Mark where platelets are.
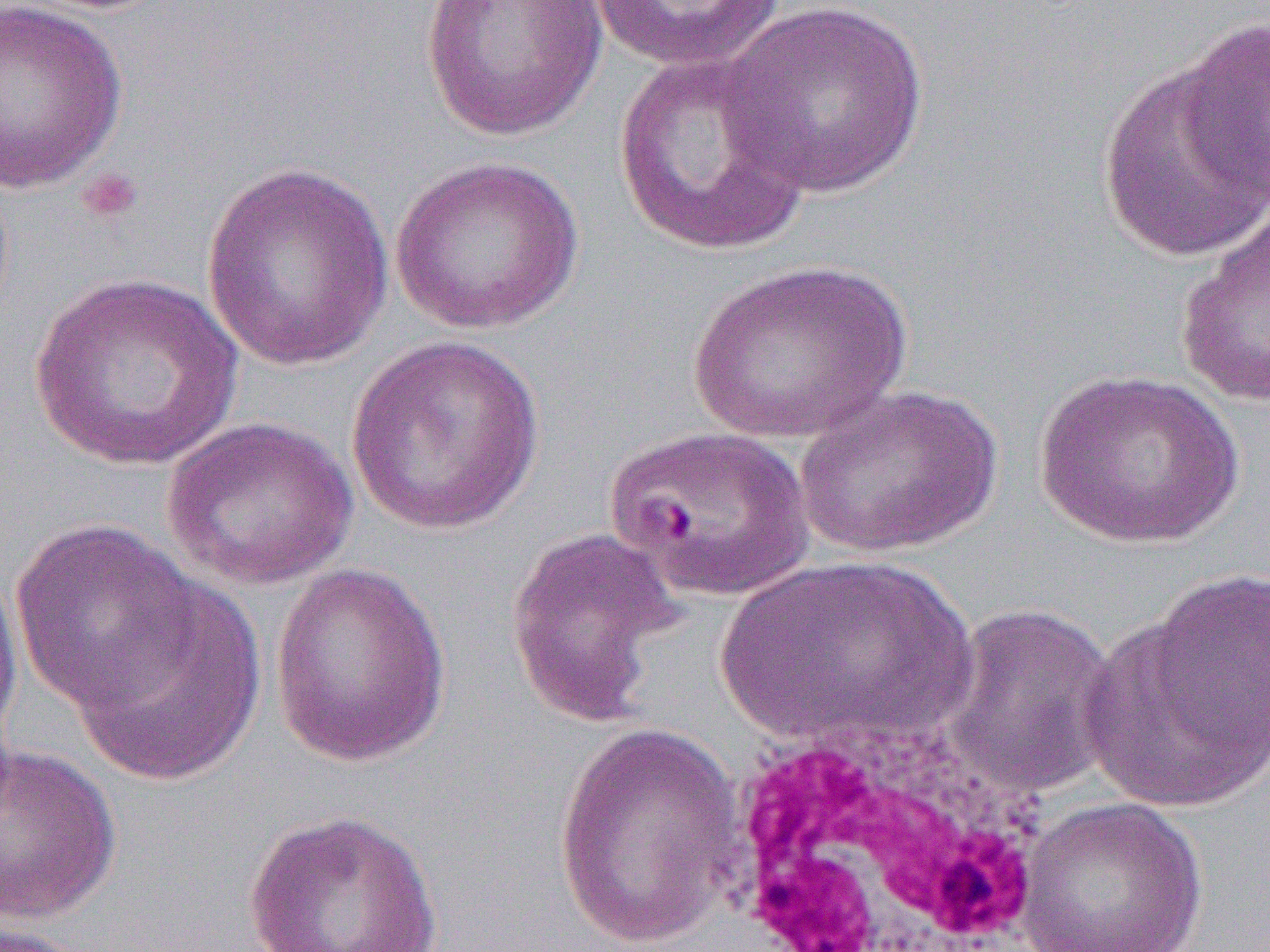

Approximate bounding boxes as (x1, y1, x2, y2) in pixels.
Platelets: (75, 166, 144, 226).

slide-level diagnosis = Plasmodium falciparum
preparation = thin blood smear
magnification = 1000x
uninfected red blood cell locations = approximate bounding boxes as (x1, y1, x2, y2) in pixels: (0, 0, 128, 194), (420, 0, 609, 142), (587, 1, 789, 72), (717, 1, 931, 199), (1176, 15, 1270, 205), (612, 52, 815, 258), (1095, 61, 1268, 267), (391, 156, 584, 334), (199, 162, 395, 372), (1173, 203, 1270, 407), (686, 257, 914, 442), (27, 273, 244, 473), (344, 336, 548, 536), (1033, 369, 1244, 549), (792, 383, 1005, 559), (161, 415, 358, 590), (604, 422, 815, 601), (11, 519, 204, 713), (504, 527, 684, 728), (718, 552, 976, 748), (0, 555, 24, 759), (269, 563, 453, 766), (68, 583, 266, 787), (1083, 587, 1268, 819), (937, 601, 1122, 802), (553, 719, 747, 952), (0, 742, 123, 923), (1015, 797, 1209, 952), (243, 809, 444, 952), (0, 920, 100, 952)
white blood cell locations = approximate bounding boxes as (x1, y1, x2, y2) in pixels: (716, 717, 1045, 952)
image size = 1270×952 pixels
modality = optical microscopy
field of view = single